Locate and identify every blood parasite.
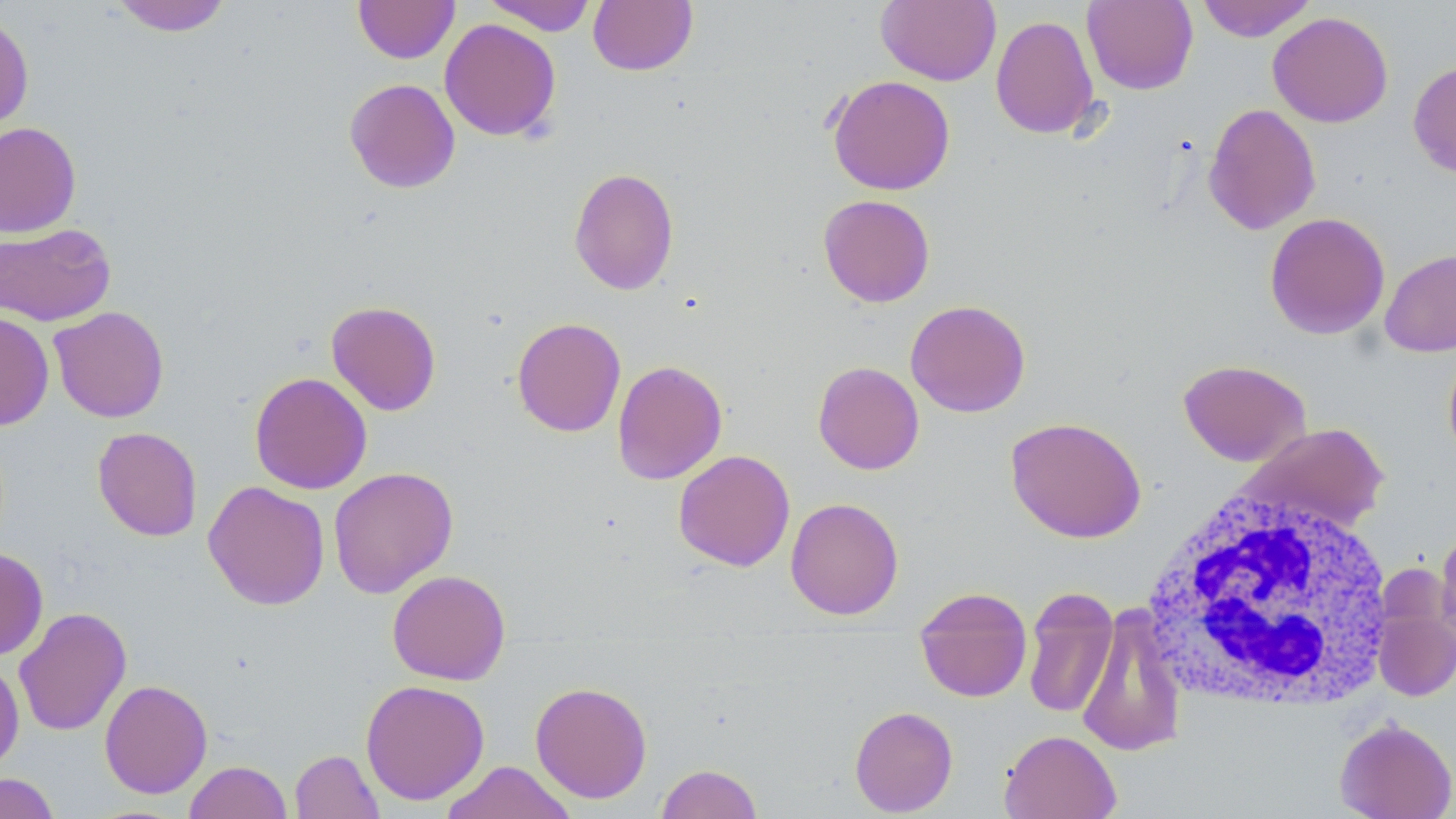
No blood parasites seen.

{
  "slide_level_diagnosis": "no evidence of blood parasites",
  "uninfected_red_blood_cell_locations": "approximate bounding boxes as (x1,y1)-(x2,y2) corner pairs in pixels: (108,0)-(234,36), (354,0)-(460,63), (482,0)-(598,35), (588,0)-(698,76), (876,0)-(1001,86), (1082,0)-(1198,94), (1196,0)-(1316,42), (0,10)-(34,132), (1268,11)-(1393,128), (990,14)-(1100,139), (439,18)-(561,142), (1408,61)-(1456,180), (827,75)-(956,195), (344,78)-(460,193), (1204,102)-(1321,235), (0,121)-(81,237), (568,167)-(679,295), (818,194)-(935,307), (1264,212)-(1390,340), (0,222)-(116,326), (1380,249)-(1456,358), (905,299)-(1031,417), (326,300)-(441,416), (48,306)-(169,423), (0,312)-(54,430), (511,317)-(626,437), (1443,345)-(1456,464), (612,359)-(728,485), (1178,359)-(1311,467), (813,361)-(924,475), (249,372)-(372,494), (1005,416)-(1147,543), (1236,422)-(1390,536), (92,426)-(202,541), (673,449)-(795,571), (328,466)-(458,598), (203,481)-(330,610), (785,497)-(904,620), (1436,526)-(1456,648), (0,547)-(49,660), (387,569)-(511,685), (914,587)-(1032,703), (1022,588)-(1119,719), (1076,604)-(1188,758), (1374,604)-(1455,701), (13,606)-(132,736), (0,657)-(24,776), (99,679)-(212,799), (360,679)-(490,805), (530,681)-(652,803), (849,705)-(958,816), (1334,717)-(1456,819), (999,729)-(1122,819), (290,749)-(384,819), (184,761)-(292,819), (439,761)-(577,819), (656,763)-(763,819), (0,772)-(60,819)",
  "white_blood_cell_locations": "approximate bounding boxes as (x1,y1)-(x2,y2) corner pairs in pixels: (1140,484)-(1397,713)",
  "modality": "light microscopy",
  "magnification": "1000x",
  "stain": "May-Grünwald-Giemsa",
  "field_of_view": "single",
  "image_size": "1456×819 pixels",
  "preparation": "thin blood film"
}